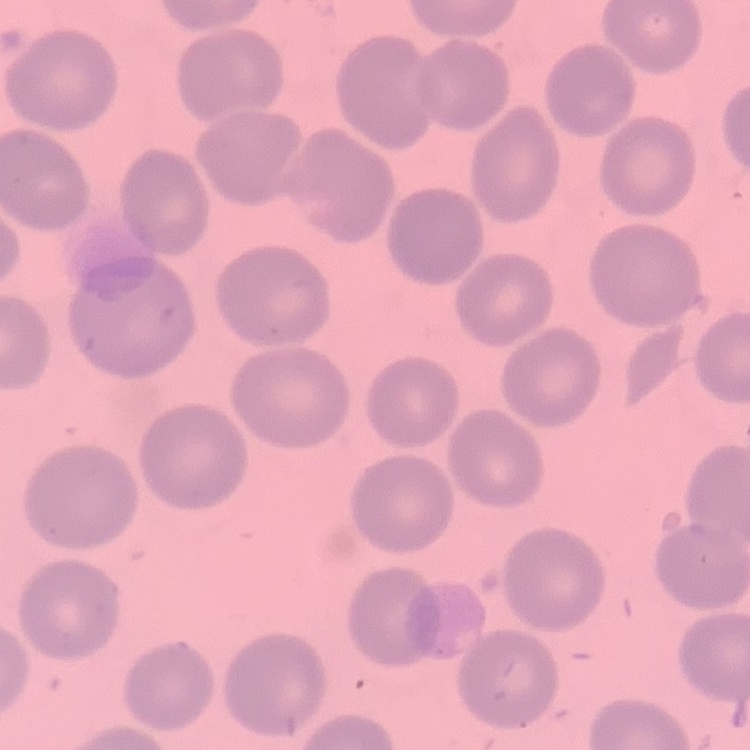
Summary:
  - Erythrocyte morphology: no rouleaux formation
  - Stain: Field's or Giemsa
  - Image type: square crop of a larger photomicrograph
  - Preparation: thin peripheral smear